Assess the morphology of the red blood cells.
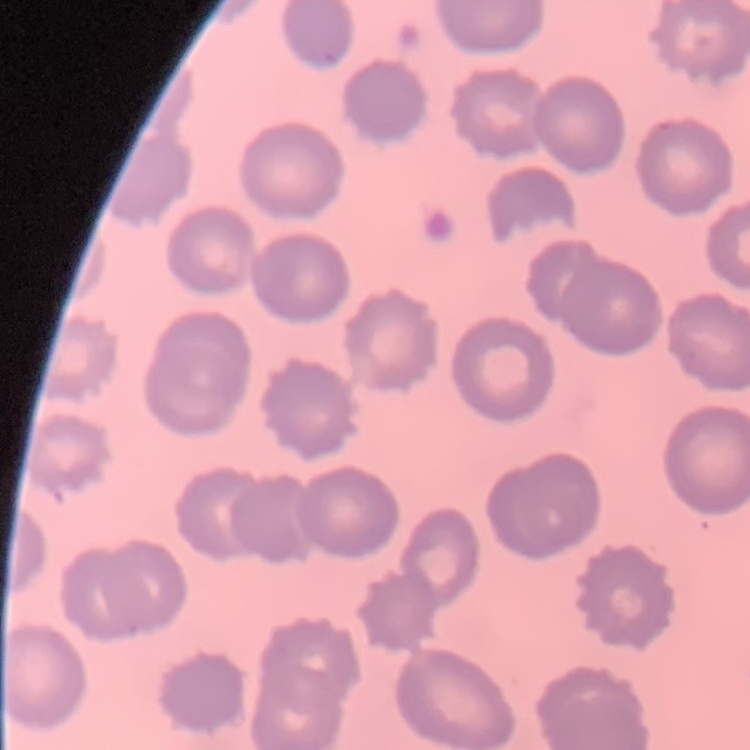

They show no rouleaux formation.

Square crop of a larger photomicrograph. Stained with either Field's or Giemsa. Thin blood smear.